Assess this cell for malaria.
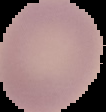
It is uninfected.

Summary:
  - Image size: 106×112 pixels
  - Image type: segmented cell region on a black background
  - Preparation: thin blood film